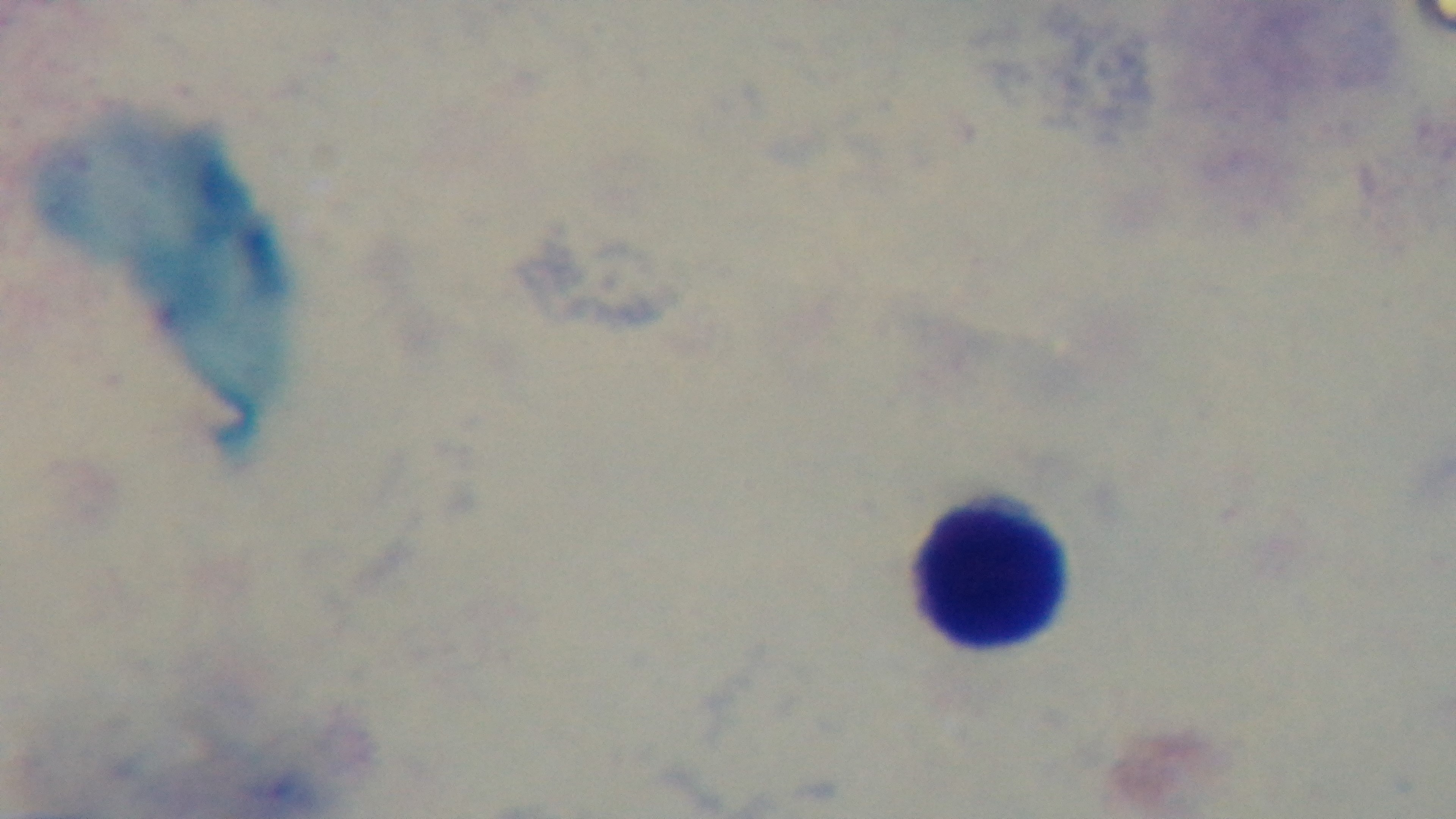

Malaria status: negative. One field from the slide. 100x oil-immersion objective. Mounted 4K digital camera. Light microscopy. Giemsa-stained. Preparation: thick smear.